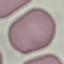
result: no malaria parasites seen
image_type: cell patch, automatically extracted from a larger field of view and resized to 64 × 64 pixels
stain: Giemsa
capture: smartphone camera at the microscope eyepiece
preparation: thin smear